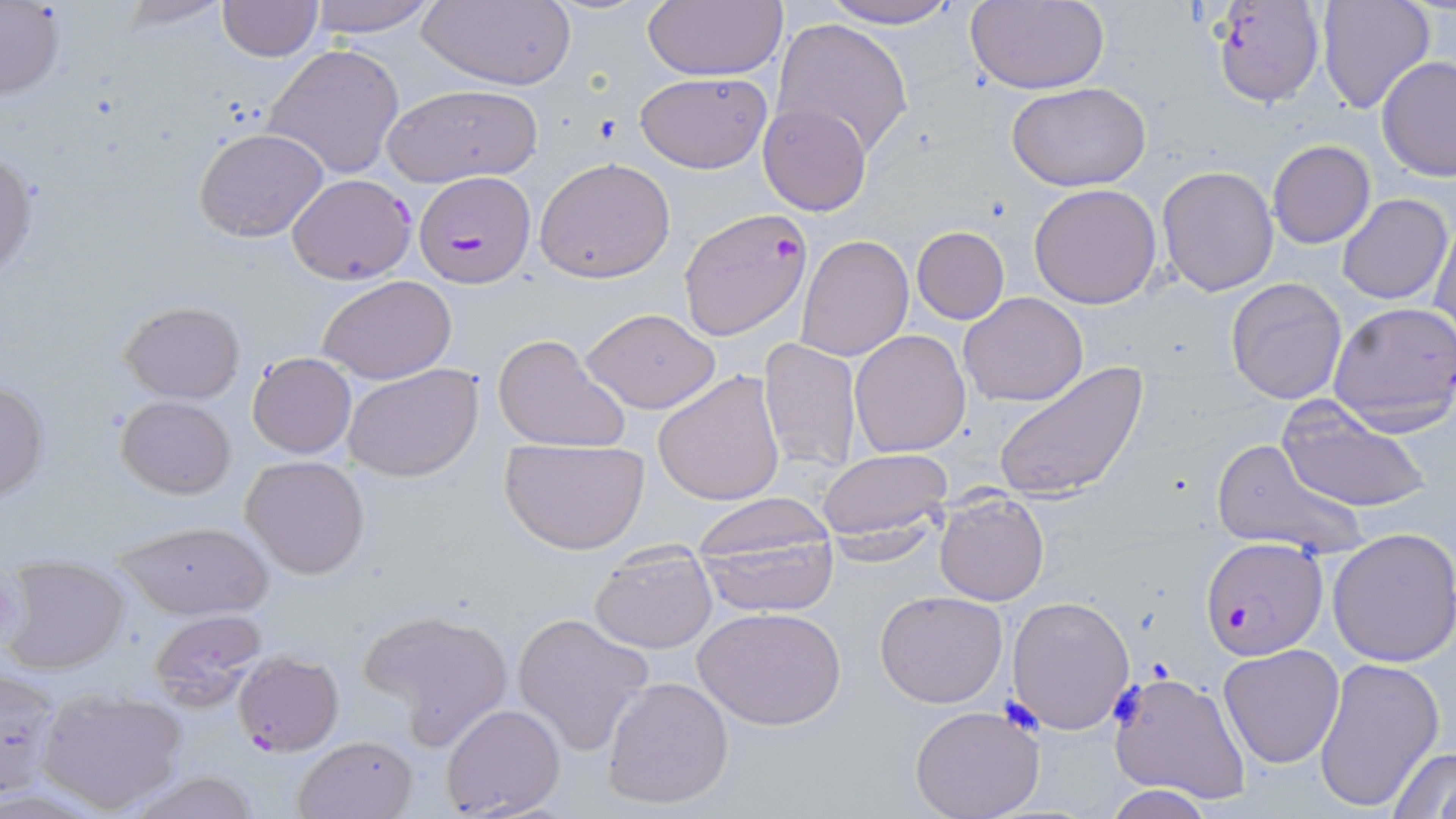
Summary:
  - Coordinate format: approximate bounding boxes as named x1/y1/x2/y2 corners in pixels
  - Plasmodium falciparum-infected red blood cell locations: (x1=1209, y1=1, x2=1326, y2=107), (x1=414, y1=172, x2=537, y2=288), (x1=677, y1=208, x2=814, y2=341), (x1=1200, y1=538, x2=1326, y2=660), (x1=231, y1=652, x2=344, y2=756)
  - Uninfected red blood cell locations: (x1=115, y1=0, x2=233, y2=32), (x1=304, y1=0, x2=437, y2=39), (x1=417, y1=0, x2=577, y2=90), (x1=642, y1=0, x2=789, y2=81), (x1=818, y1=0, x2=967, y2=30), (x1=1316, y1=0, x2=1437, y2=114), (x1=217, y1=1, x2=322, y2=61), (x1=964, y1=2, x2=1110, y2=92), (x1=0, y1=4, x2=67, y2=101), (x1=771, y1=17, x2=913, y2=156), (x1=263, y1=43, x2=407, y2=181), (x1=1377, y1=56, x2=1456, y2=182), (x1=633, y1=71, x2=773, y2=174), (x1=1007, y1=81, x2=1151, y2=192), (x1=382, y1=83, x2=544, y2=186), (x1=758, y1=102, x2=871, y2=216), (x1=193, y1=128, x2=330, y2=244), (x1=1266, y1=140, x2=1377, y2=249), (x1=0, y1=150, x2=38, y2=286), (x1=534, y1=157, x2=677, y2=283), (x1=1155, y1=165, x2=1281, y2=296), (x1=287, y1=173, x2=416, y2=284), (x1=1029, y1=183, x2=1162, y2=308), (x1=1337, y1=194, x2=1453, y2=305), (x1=1431, y1=216, x2=1456, y2=340), (x1=910, y1=227, x2=1010, y2=324), (x1=795, y1=235, x2=914, y2=361), (x1=318, y1=276, x2=456, y2=384), (x1=1225, y1=276, x2=1348, y2=405), (x1=959, y1=292, x2=1089, y2=407), (x1=120, y1=300, x2=246, y2=402), (x1=1327, y1=302, x2=1456, y2=435), (x1=580, y1=306, x2=721, y2=414), (x1=849, y1=330, x2=971, y2=457), (x1=492, y1=333, x2=632, y2=455), (x1=757, y1=337, x2=861, y2=474), (x1=247, y1=353, x2=356, y2=458), (x1=992, y1=362, x2=1147, y2=503), (x1=342, y1=363, x2=482, y2=483), (x1=652, y1=370, x2=786, y2=506), (x1=0, y1=379, x2=50, y2=502), (x1=1276, y1=395, x2=1433, y2=515), (x1=117, y1=396, x2=236, y2=498), (x1=500, y1=436, x2=650, y2=555), (x1=1210, y1=438, x2=1366, y2=559), (x1=817, y1=448, x2=953, y2=550), (x1=240, y1=456, x2=370, y2=578), (x1=935, y1=491, x2=1049, y2=606), (x1=691, y1=498, x2=840, y2=616), (x1=113, y1=518, x2=271, y2=619), (x1=1327, y1=527, x2=1456, y2=667), (x1=589, y1=542, x2=718, y2=654), (x1=2, y1=555, x2=130, y2=675), (x1=875, y1=591, x2=1007, y2=708), (x1=1007, y1=595, x2=1135, y2=735), (x1=695, y1=605, x2=846, y2=731), (x1=356, y1=607, x2=513, y2=744), (x1=149, y1=610, x2=270, y2=713), (x1=511, y1=611, x2=656, y2=756), (x1=1218, y1=643, x2=1346, y2=768), (x1=1312, y1=656, x2=1444, y2=814), (x1=1, y1=666, x2=65, y2=797), (x1=1108, y1=670, x2=1252, y2=806), (x1=602, y1=676, x2=735, y2=810), (x1=36, y1=685, x2=189, y2=813), (x1=440, y1=703, x2=566, y2=818), (x1=909, y1=706, x2=1045, y2=819), (x1=292, y1=735, x2=418, y2=819), (x1=1386, y1=744, x2=1456, y2=819), (x1=120, y1=770, x2=262, y2=819), (x1=1104, y1=785, x2=1225, y2=818)
  - Slide-level diagnosis: Plasmodium falciparum
  - Preparation: thin blood smear
  - Stain: May-Grünwald-Giemsa
  - Modality: light microscopy
  - Magnification: 1000x
  - Field of view: one of a larger specimen
  - Image size: 1456×819 pixels